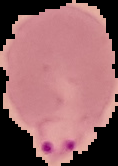
image type = segmented cell region with the area outside set to black
malaria status = parasitized
preparation = thin blood smear
image size = 118×166 pixels